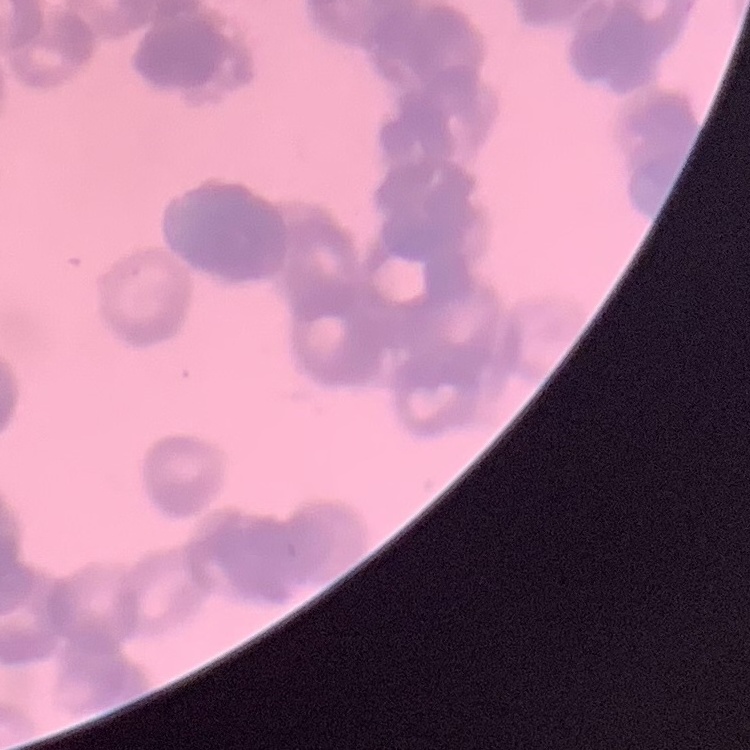 The erythrocytes show rouleaux formation. Field's or Giemsa stain. Thin blood film. Square crop of a larger photomicrograph.